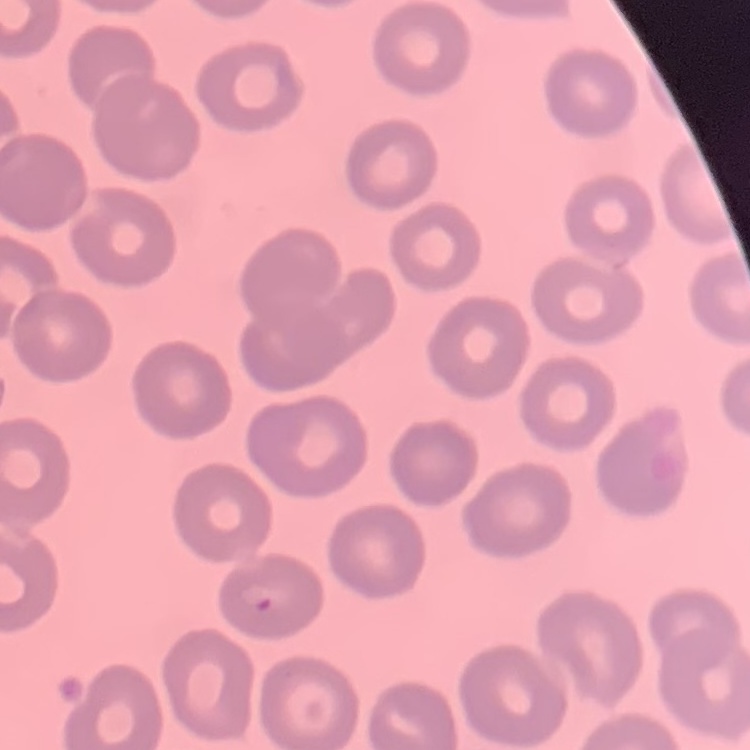
Summary:
  - Erythrocyte morphology: no rouleaux formation
  - Stain: Field's or Giemsa
  - Preparation: thin blood smear
  - Image type: square crop of a larger photomicrograph